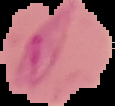
Summary:
  - Result: Plasmodium parasites detected
  - Image type: segmented cell region with the area outside set to black
  - Preparation: thin blood smear
  - Image size: 115×106 pixels